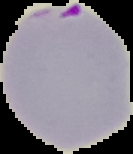

result = Plasmodium parasites identified
image type = segmented cell region with the area outside set to black
preparation = thin blood smear
image size = 133×154 pixels